Report the malaria status of this cell.
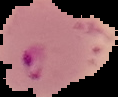

It is parasitized.

From a thin blood film. Image is 118×97 pixels. Cell region segmented out of the field of view; the surrounding area is masked to black.